Comment on the background quality.
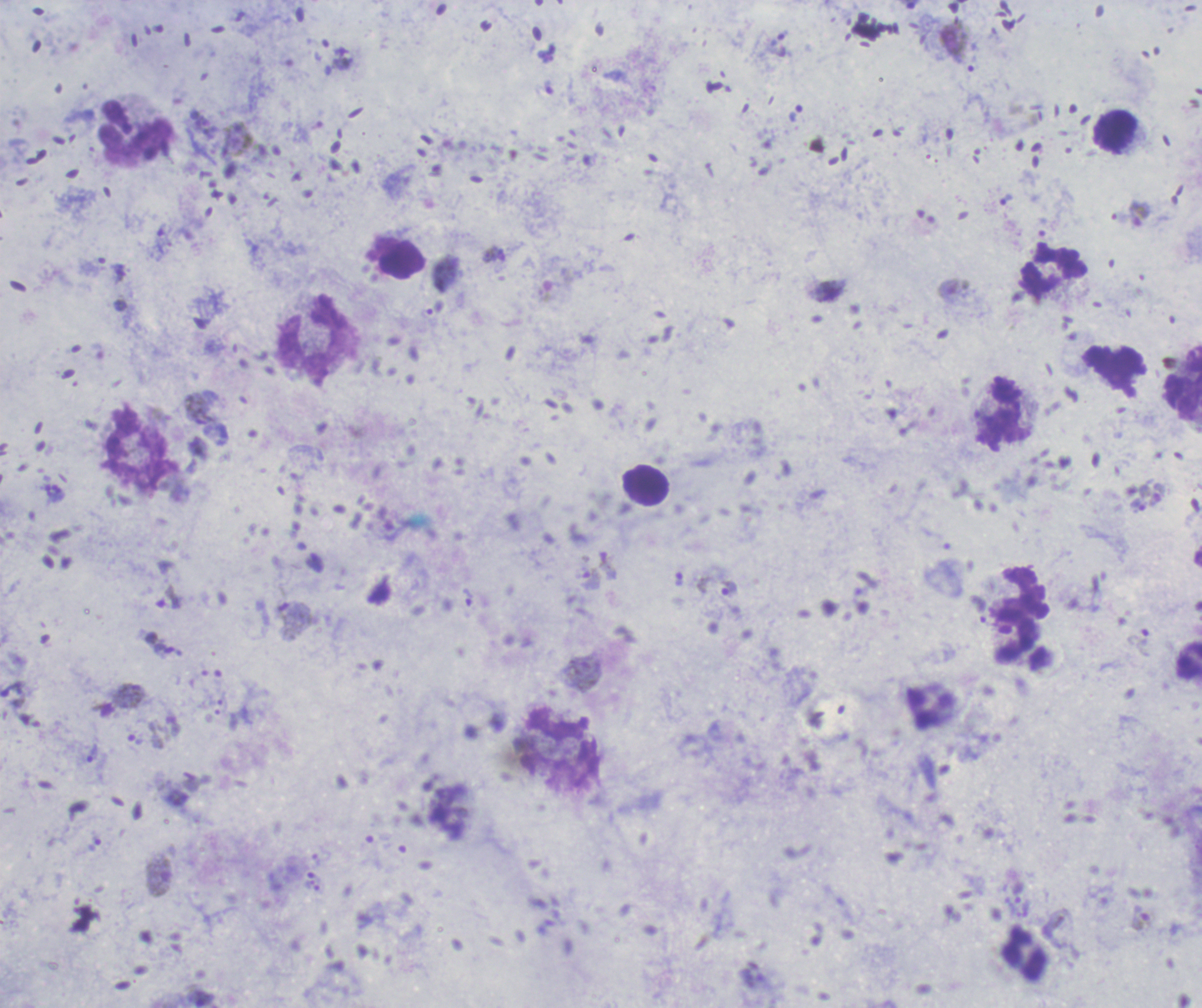
It is good.

Approximate object centers, in pixels from the top-left corner.
Summary:
  - Gametocyte locations: (x=1139, y=213), (x=608, y=566), (x=588, y=577), (x=295, y=621), (x=122, y=700), (x=158, y=876), (x=1142, y=919)
  - Leukocyte locations: (x=1116, y=131), (x=134, y=133), (x=1052, y=271), (x=315, y=344), (x=1183, y=383), (x=1002, y=412), (x=136, y=450), (x=645, y=486), (x=1018, y=591), (x=1188, y=661), (x=558, y=748), (x=1024, y=955)
  - Trophozoite locations: (x=488, y=255), (x=728, y=588), (x=168, y=597), (x=1138, y=644), (x=145, y=736), (x=92, y=753)
  - Life-cycle stages observed: trophozoite, gametocyte
  - Image size: 1202×1008 pixels
  - Magnification: 100x
  - Context: previously used in an actual diagnosis
  - Field of view: single
  - Preparation: thick blood smear
  - Result: positive for Plasmodium parasites
  - Stain: Romanowsky